Assess this cell for malaria.
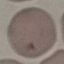
Uninfected.

image type = cell patch, automatically extracted from a larger field of view and resized to 64 × 64 pixels
stain = Giemsa
preparation = thin blood smear
capture = smartphone through the microscope eyepiece